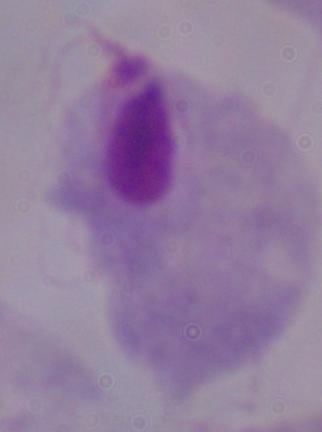

Micrograph. A trichomonad is shown. 1000x magnification.